Report the malaria status of this cell.
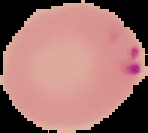
It is parasitized.

image size = 148×133 pixels
image type = cell region segmented out of the field of view; surrounding area masked to black
preparation = thin blood film